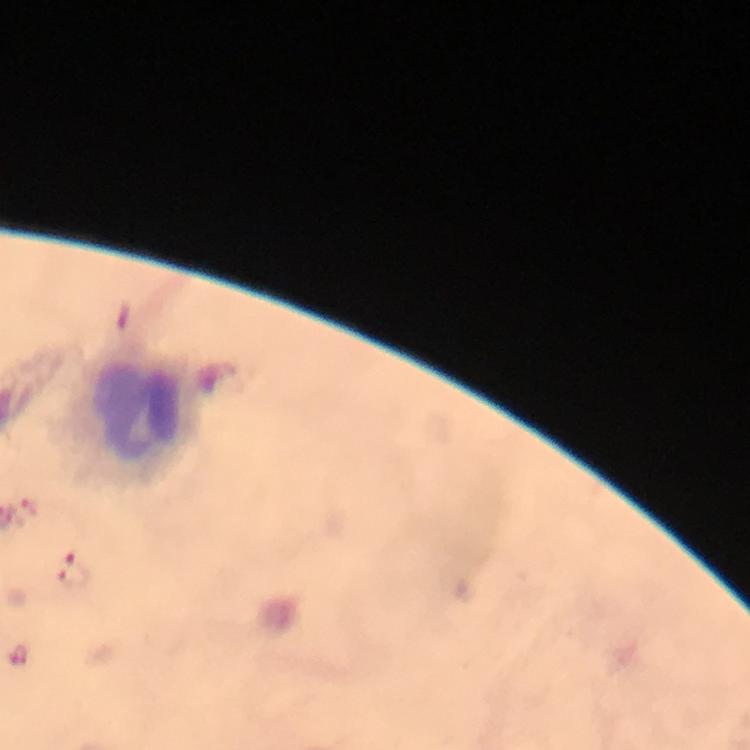
Approximate object centers, in pixels from the top-left corner.
Summary:
  - Malaria parasite locations: (x=30, y=504), (x=72, y=569), (x=18, y=658)
  - Leukocyte locations: (x=135, y=416)
  - Context: from a malaria diagnostic workup
  - Image size: 750×750 pixels
  - Cropped from: one field of view
  - Preparation: thick blood smear
  - Magnification: 100x
  - Immersion oil: applied
  - Capture: smartphone camera through the microscope
  - Stain: Giemsa